Report the malaria status of this cell.
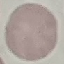

It is uninfected.

Automatically extracted cell patch, resized to 64 × 64 pixels. Photographed with a smartphone camera at the microscope eyepiece. Giemsa-stained preparation. Thin blood film.